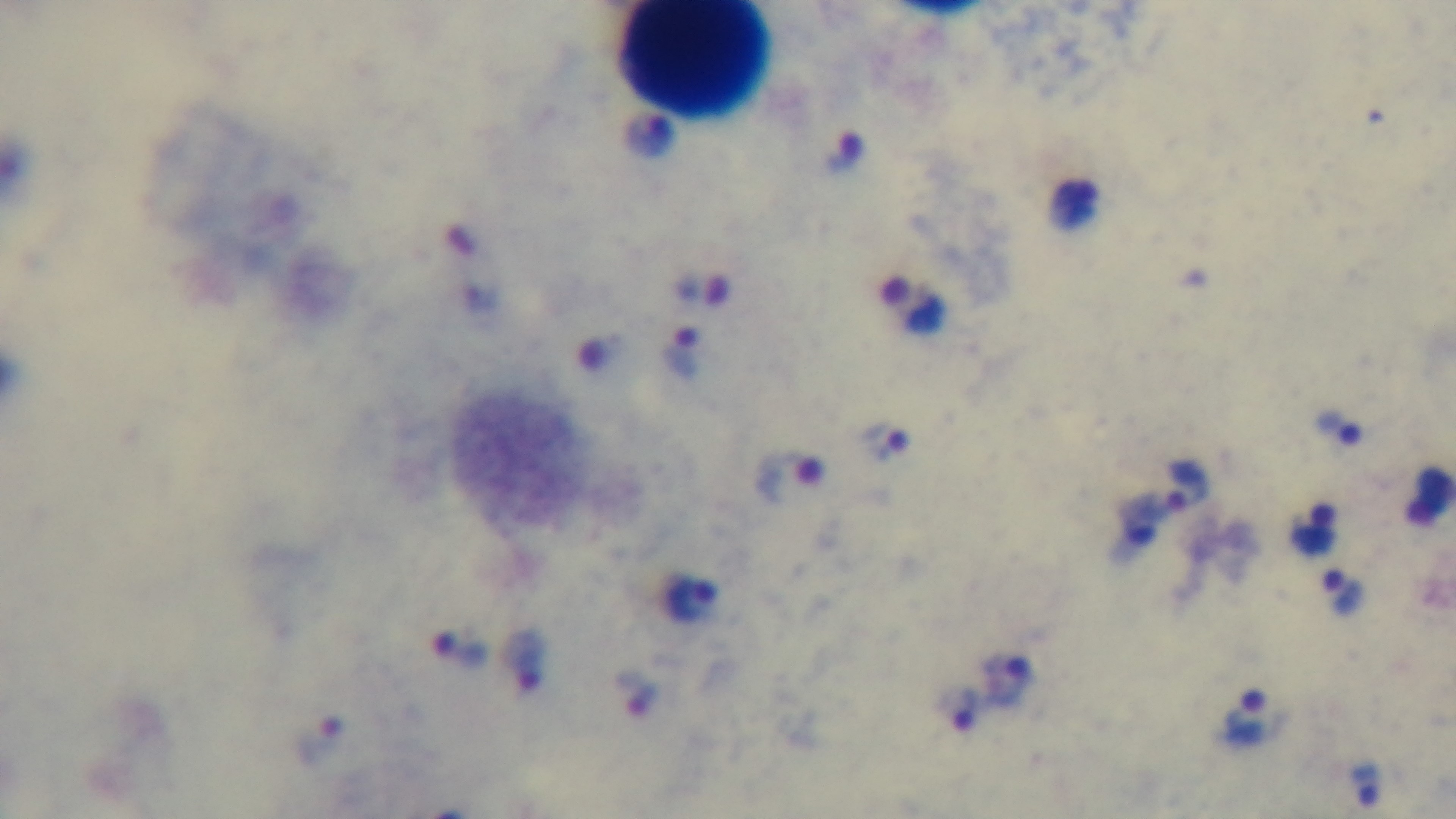 Single field of view. Preparation: thick blood film. Photomicrograph. Malaria status: infected. 100x oil-immersion objective. Captured with a mounted 4K digital camera. Giemsa-stained.